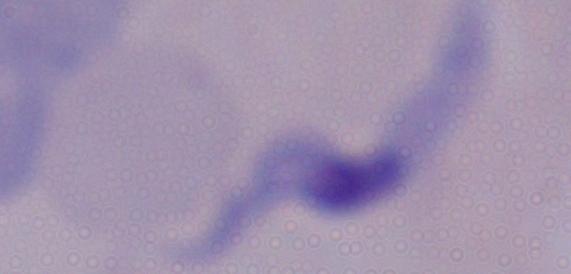
modality = photomicrograph
magnification = 1000x
identification = trypanosome